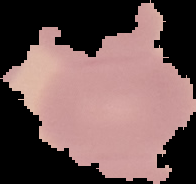
Summary:
  - Image type: segmented cell region on a black background
  - Preparation: thin blood smear
  - Malaria status: uninfected
  - Image size: 196×184 pixels